Report the malaria status of this cell.
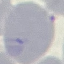
Uninfected.

stain = Giemsa
image type = cell patch, automatically extracted from a larger field of view and resized to 64 × 64 pixels
preparation = thin blood film
capture = smartphone camera at the microscope eyepiece